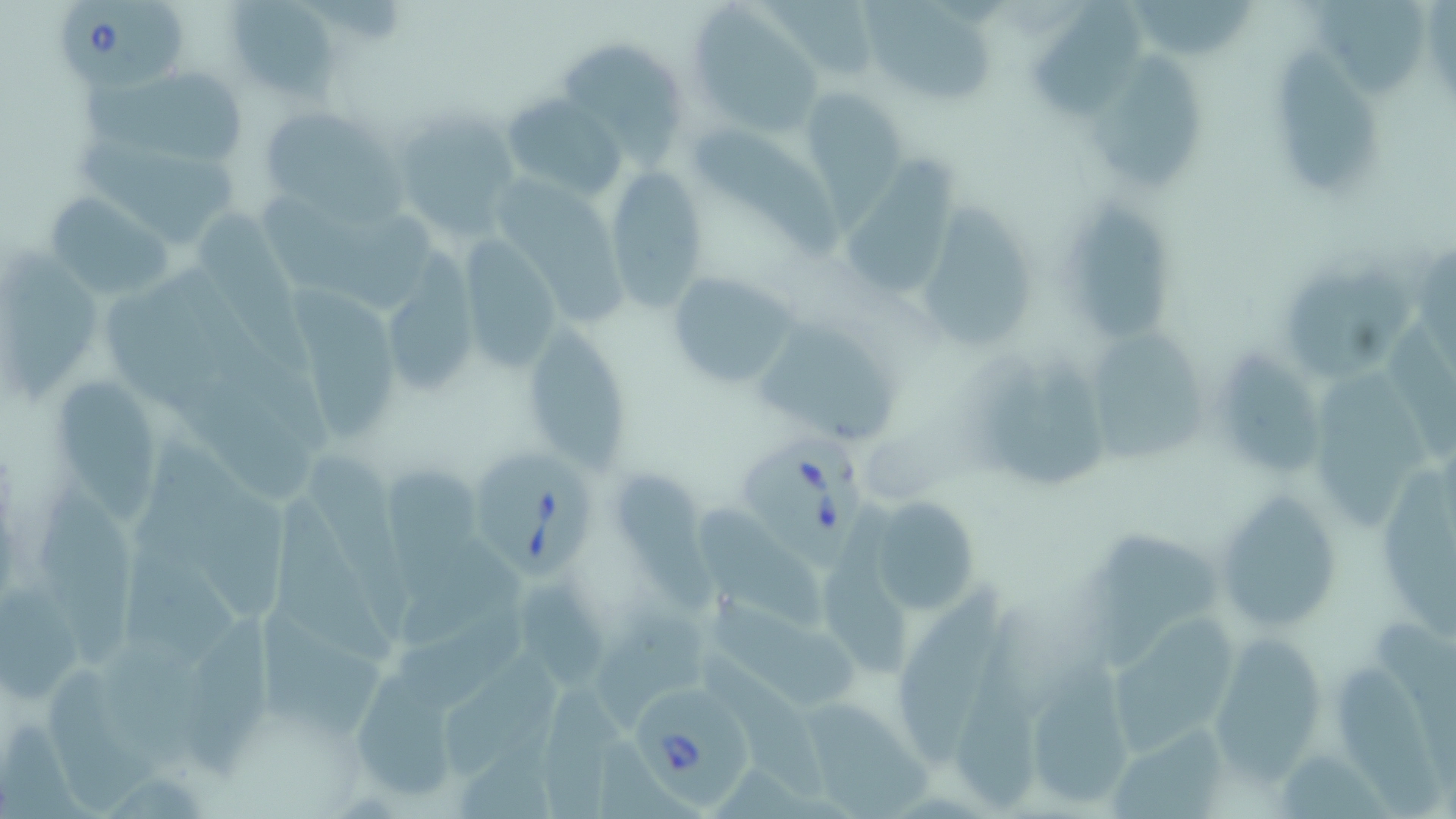

slide_level_diagnosis: Babesia divergens
modality: light microscopy
uninfected_red_blood_cell_locations: 'approximate bounding boxes as (x1, y1, x2, y2) in pixels: (224, 0, 341, 102), (766, 0, 888, 87), (1023, 0, 1152, 128), (1140, 0, 1259, 64), (866, 2, 997, 107), (1307, 5, 1426, 96), (688, 10, 821, 135), (559, 39, 684, 171), (1094, 45, 1196, 197), (1268, 50, 1381, 194), (75, 69, 249, 162), (800, 87, 906, 198), (501, 92, 626, 199), (260, 104, 399, 212), (389, 108, 523, 237), (687, 124, 843, 263), (70, 132, 238, 250), (843, 157, 958, 296), (603, 165, 710, 310), (502, 184, 630, 327), (1058, 187, 1173, 345), (45, 192, 177, 301), (271, 194, 443, 306), (918, 198, 1035, 351), (206, 214, 319, 374), (0, 238, 100, 413), (458, 238, 563, 371), (1408, 244, 1456, 353), (1273, 258, 1412, 383), (168, 266, 335, 447), (666, 270, 801, 389), (381, 273, 478, 400), (290, 286, 403, 445), (100, 287, 306, 494), (756, 319, 895, 447), (1385, 323, 1456, 464), (520, 325, 634, 473), (1094, 328, 1207, 465), (1223, 340, 1325, 480), (974, 355, 1107, 492), (1312, 375, 1430, 528), (55, 376, 157, 529), (136, 439, 294, 620), (301, 447, 415, 640), (617, 466, 715, 610), (1376, 470, 1456, 632), (382, 475, 489, 599), (33, 481, 135, 672), (1215, 489, 1340, 636), (271, 496, 400, 669), (869, 496, 981, 616), (703, 509, 835, 629), (1087, 527, 1216, 667), (521, 570, 610, 687), (892, 579, 998, 762), (1, 580, 88, 706), (402, 592, 544, 710), (709, 595, 867, 711), (186, 603, 279, 783), (602, 603, 709, 732), (1366, 603, 1456, 777), (249, 607, 385, 733), (953, 613, 1055, 804), (1110, 618, 1241, 744), (101, 638, 215, 774), (1211, 640, 1324, 779), (443, 650, 562, 772), (705, 655, 826, 801), (1335, 659, 1443, 818), (43, 662, 165, 811), (1023, 671, 1133, 810), (352, 676, 463, 804), (537, 677, 623, 818), (806, 698, 940, 815)'
stain: May-Grünwald-Giemsa
babesia_divergens_infected_red_blood_cell_locations: 'approximate bounding boxes as (x1, y1, x2, y2) in pixels: (54, 2, 192, 94), (738, 432, 869, 576), (471, 449, 599, 581), (628, 676, 759, 807)'
field_of_view: one of a larger specimen
magnification: 1000x
preparation: thin blood smear
image_size: 1456×819 pixels